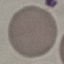 Result: no malaria parasites seen. Photographed with a smartphone camera at the microscope eyepiece. Cell patch, automatically extracted from a larger field of view and resized to 64 × 64 pixels. Thin blood smear. Giemsa stain.